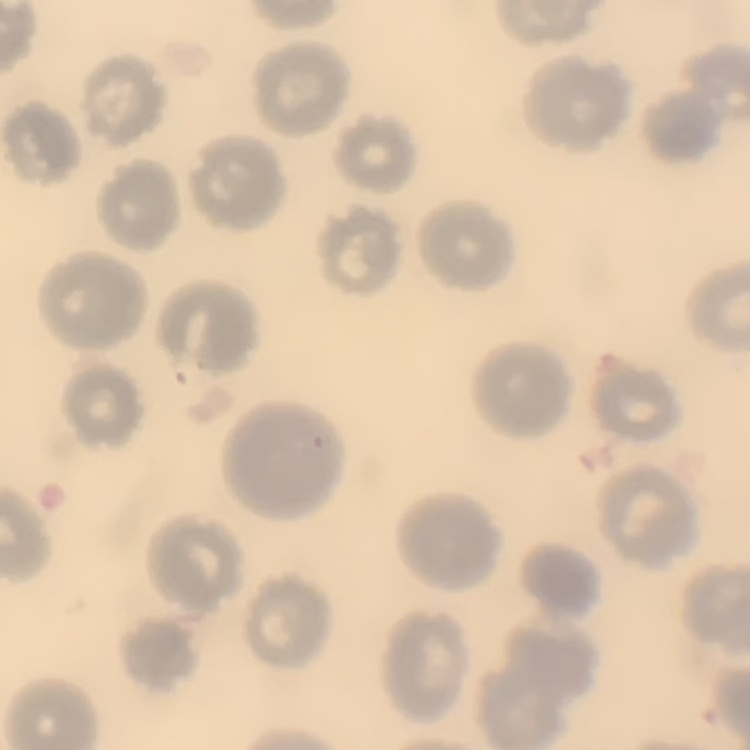
red_blood_cell_morphology: no rouleaux formation
image_type: square crop of a larger photomicrograph
stain: Field's or Giemsa
preparation: thin blood smear